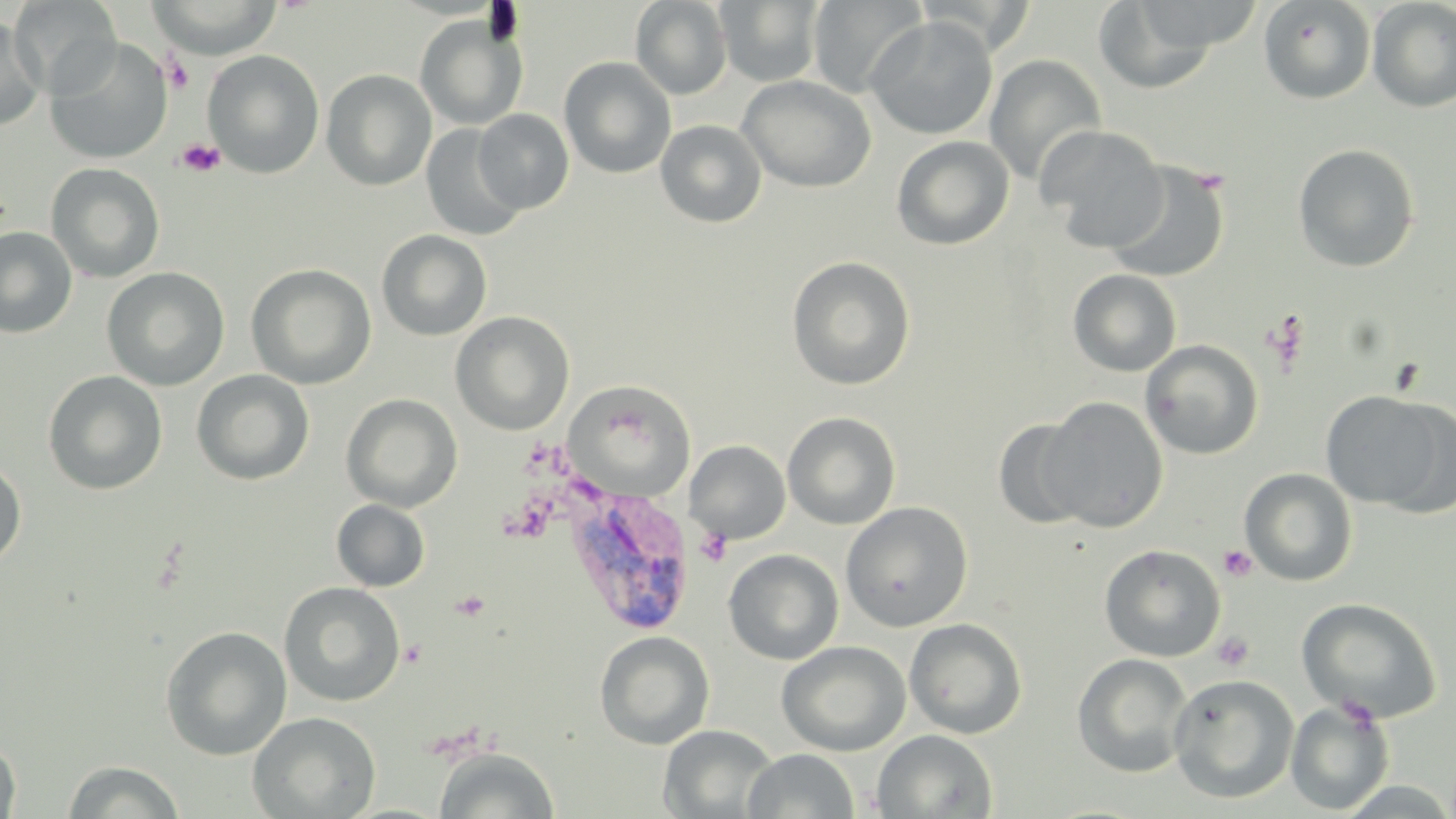

slide_level_diagnosis: Plasmodium vivax
uninfected_red_blood_cell_locations: 'approximate bounding boxes as [x1, y1, x2, y2] in pixels: [8, 0, 122, 98], [807, 0, 927, 98], [913, 0, 1039, 56], [1257, 0, 1376, 105], [145, 1, 282, 59], [630, 1, 732, 100], [715, 1, 826, 86], [1091, 1, 1228, 95], [1367, 1, 1456, 113], [415, 14, 527, 131], [864, 16, 998, 140], [0, 17, 46, 132], [44, 37, 173, 164], [202, 50, 325, 178], [984, 54, 1107, 187], [559, 57, 676, 178], [321, 69, 436, 190], [737, 75, 876, 193], [473, 109, 574, 213], [655, 119, 767, 228], [421, 123, 527, 241], [1038, 125, 1170, 252], [891, 135, 1015, 250], [1293, 143, 1420, 273], [1104, 160, 1230, 284], [45, 162, 166, 283], [0, 226, 77, 339], [377, 230, 493, 341], [786, 256, 916, 390], [246, 263, 376, 389], [101, 267, 230, 391], [1068, 269, 1182, 377], [450, 311, 575, 435], [1140, 339, 1264, 460], [191, 369, 314, 486], [43, 370, 167, 495], [565, 382, 696, 497], [1319, 389, 1453, 513], [341, 393, 463, 512], [1039, 397, 1169, 533], [782, 411, 901, 530], [991, 417, 1094, 530], [686, 440, 790, 544], [0, 459, 27, 568], [1240, 468, 1357, 587], [331, 499, 430, 591], [840, 501, 974, 632], [1099, 544, 1226, 662], [723, 548, 844, 665], [279, 581, 406, 707], [1295, 597, 1443, 723], [904, 617, 1028, 739], [160, 626, 292, 760], [594, 630, 715, 750], [777, 641, 911, 756], [1073, 653, 1194, 778], [1168, 673, 1300, 804], [1285, 699, 1395, 815], [247, 711, 382, 818], [658, 725, 779, 818], [872, 729, 997, 818], [0, 736, 21, 819], [434, 746, 559, 818], [743, 748, 860, 818], [60, 760, 186, 819]'
stain: May-Grünwald-Giemsa
plasmodium_vivax_infected_red_blood_cell_locations: 'approximate bounding boxes as [x1, y1, x2, y2] in pixels: [562, 486, 697, 638]'
image_size: 1456×819 pixels
modality: light microscopy
preparation: thin blood film
field_of_view: one of a larger specimen
platelet_locations: 'approximate bounding boxes as [x1, y1, x2, y2] in pixels: [162, 56, 195, 93], [175, 137, 225, 178], [1262, 308, 1311, 374], [694, 528, 732, 566], [1218, 545, 1258, 582], [1211, 631, 1255, 672]'
magnification: 1000x